Describe the morphology of the erythrocytes.
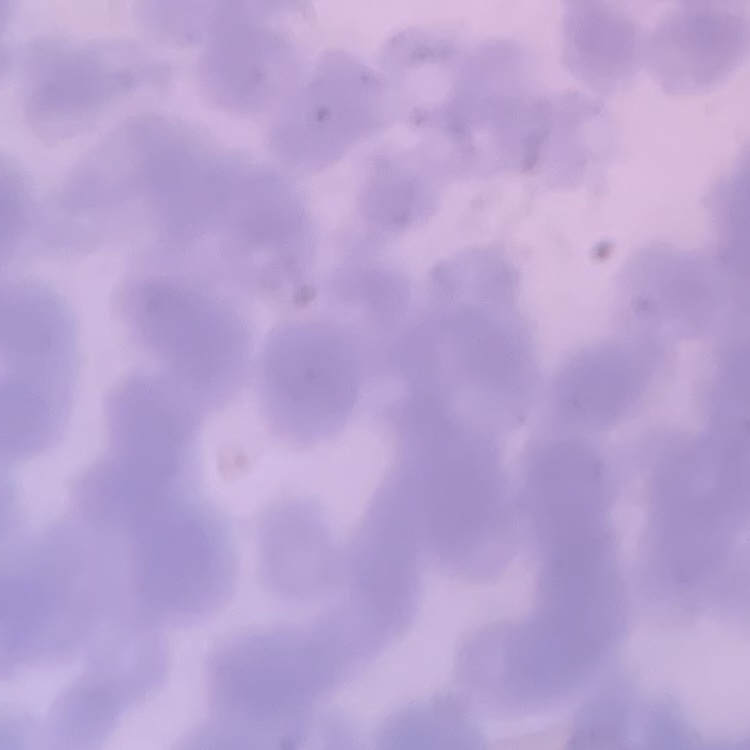

They show rouleaux formation.

image type = one tile cut from a larger photomicrograph
preparation = thin blood film
stain = Field's or Giemsa